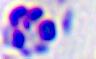
Summary:
  - Modality: photomicrograph
  - Identification: white blood cell
  - Magnification: 400x